Identify the parasite.
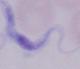
This is a trypanosome.

Summary:
  - Magnification: 1000x
  - Modality: photomicrograph